Give the extent of the malaria parasites you find, grouped by life-cycle stage — ring form, trophozoite, schizont, or gametocyte.
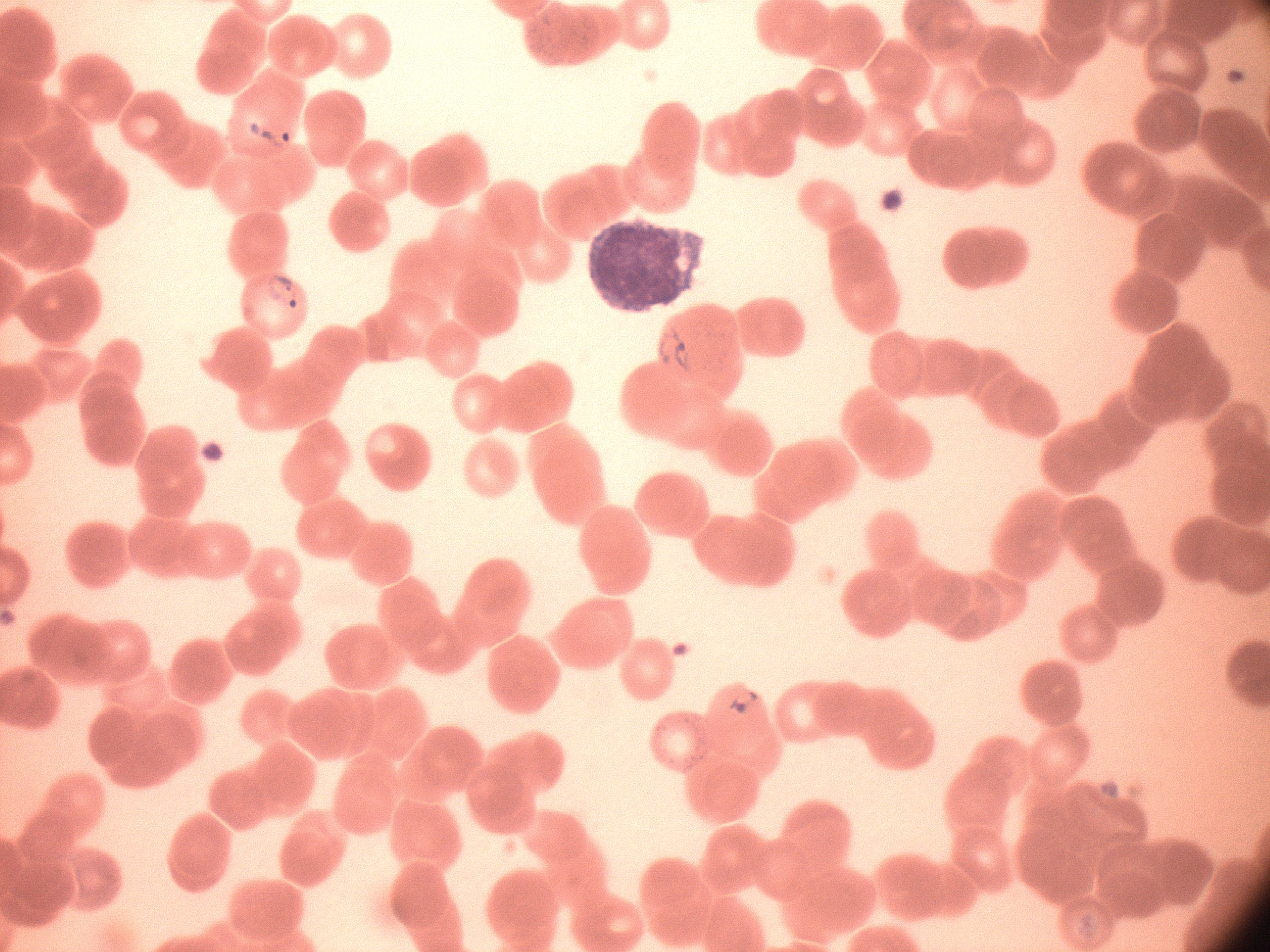

Approximate bounding boxes as (x1,y1)-(x2,y2) corner pairs in pixels, from the source annotation, which is not necessarily exhaustive.
Ring forms: (237,106)-(297,160), (261,267)-(311,315), (649,322)-(697,382), (723,683)-(763,724).

Summary:
  - Stain: Giemsa
  - Species: Plasmodium falciparum
  - Image size: 1270×952 pixels
  - Microscope: Leica DM2000 with built-in camera
  - Magnification: 100x
  - Field of view: one from this slide
  - Preparation: thin blood smear